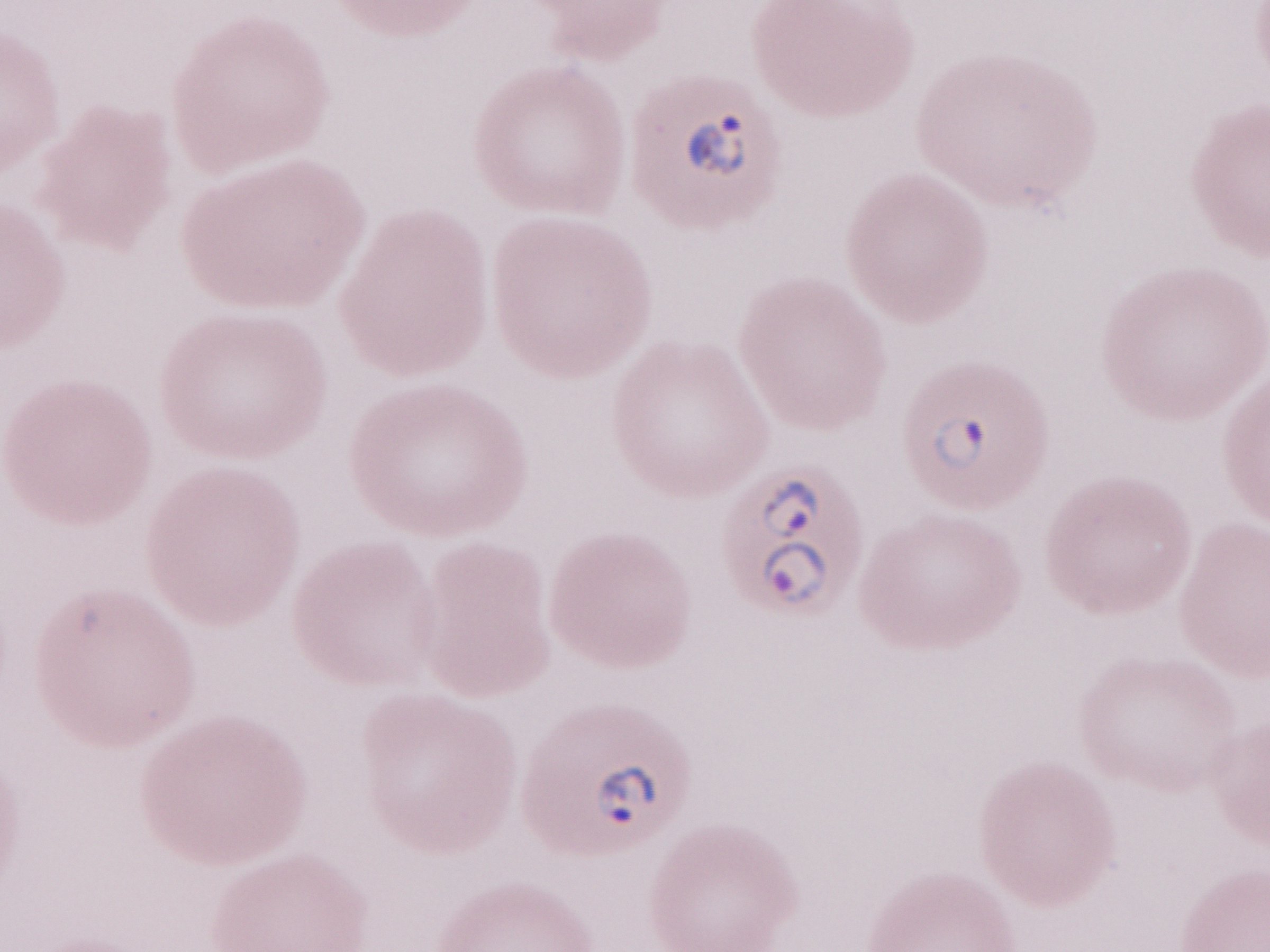

Thin peripheral-blood smear. Olympus BX43 microscope and DP73 digital camera. Image is 1270×952 pixels. Patient diagnosis: malaria infection. May-Grünwald-Giemsa-stained preparation. 1,000x magnification. Single field of view.